Identify the preparation type.
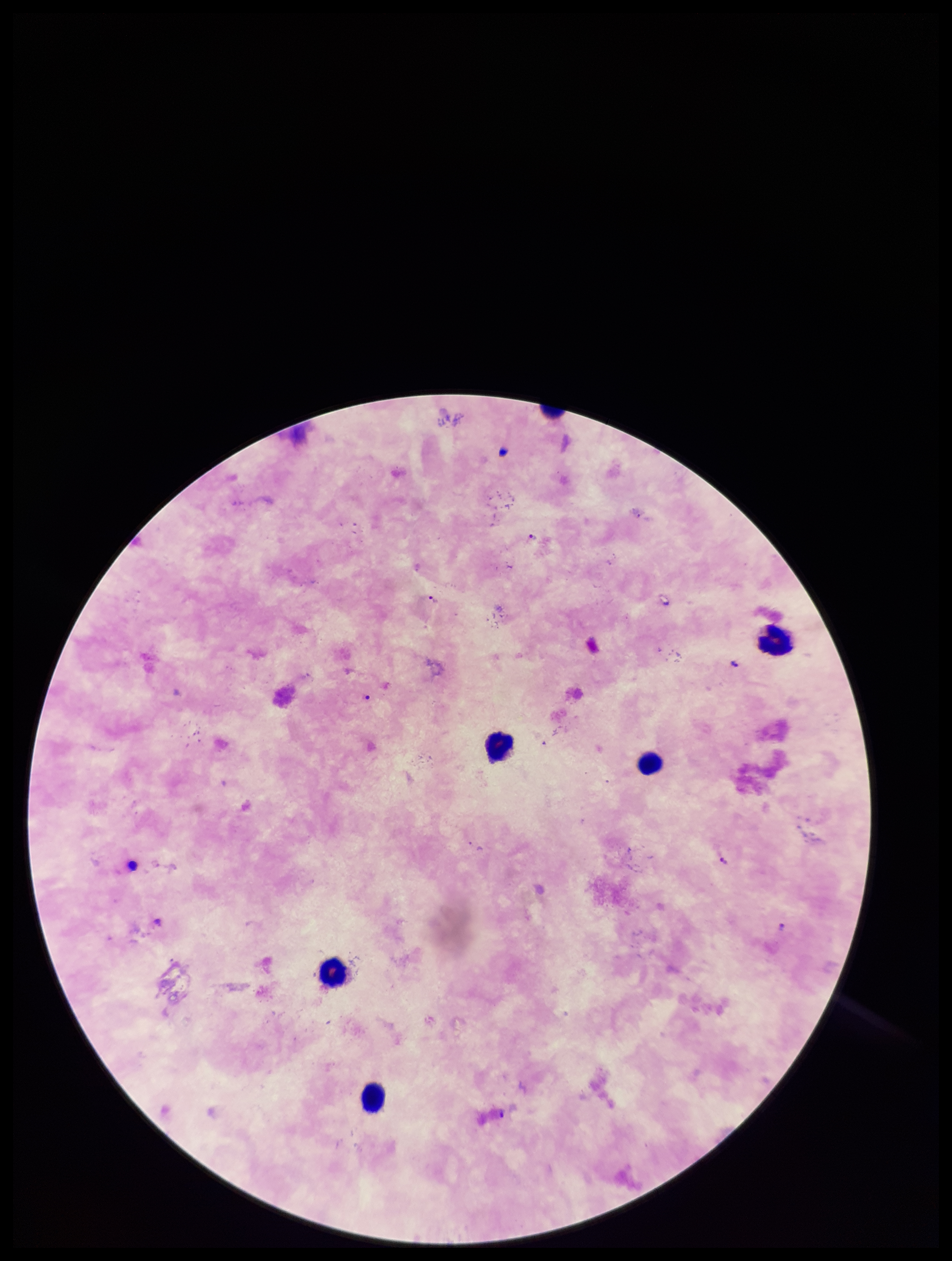
Thick.

capture = smartphone photograph through the microscope eyepiece
stain = Giemsa
species reported for this patient = Plasmodium falciparum
field of view = one from this slide
leukocyte count = 5
patient malaria status = infected
parasite count = 4
Plasmodium parasites = identified
image size = 952×1261 pixels